Assess this cell for malaria.
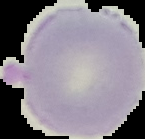
Uninfected.

Summary:
  - Image type: segmented cell region on a black background
  - Image size: 145×139 pixels
  - Preparation: thin blood film